Assess the morphology of the erythrocytes.
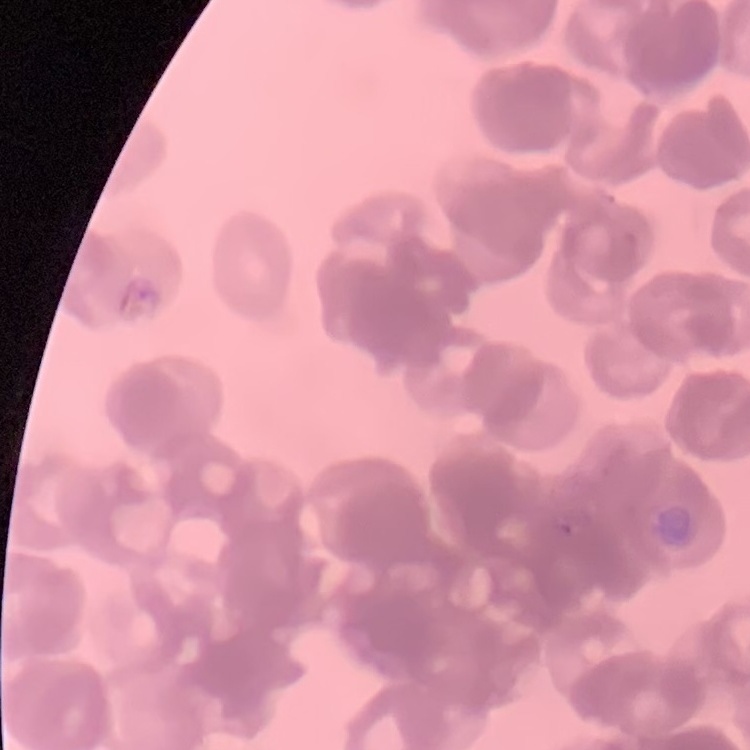

They show rouleaux formation.

Square crop of a larger photomicrograph. Field's or Giemsa stain. Thin blood smear.